State which parasite is depicted.
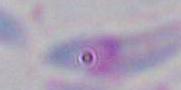

This is Toxoplasma gondii.

Summary:
  - Magnification: 1000x
  - Modality: micrograph